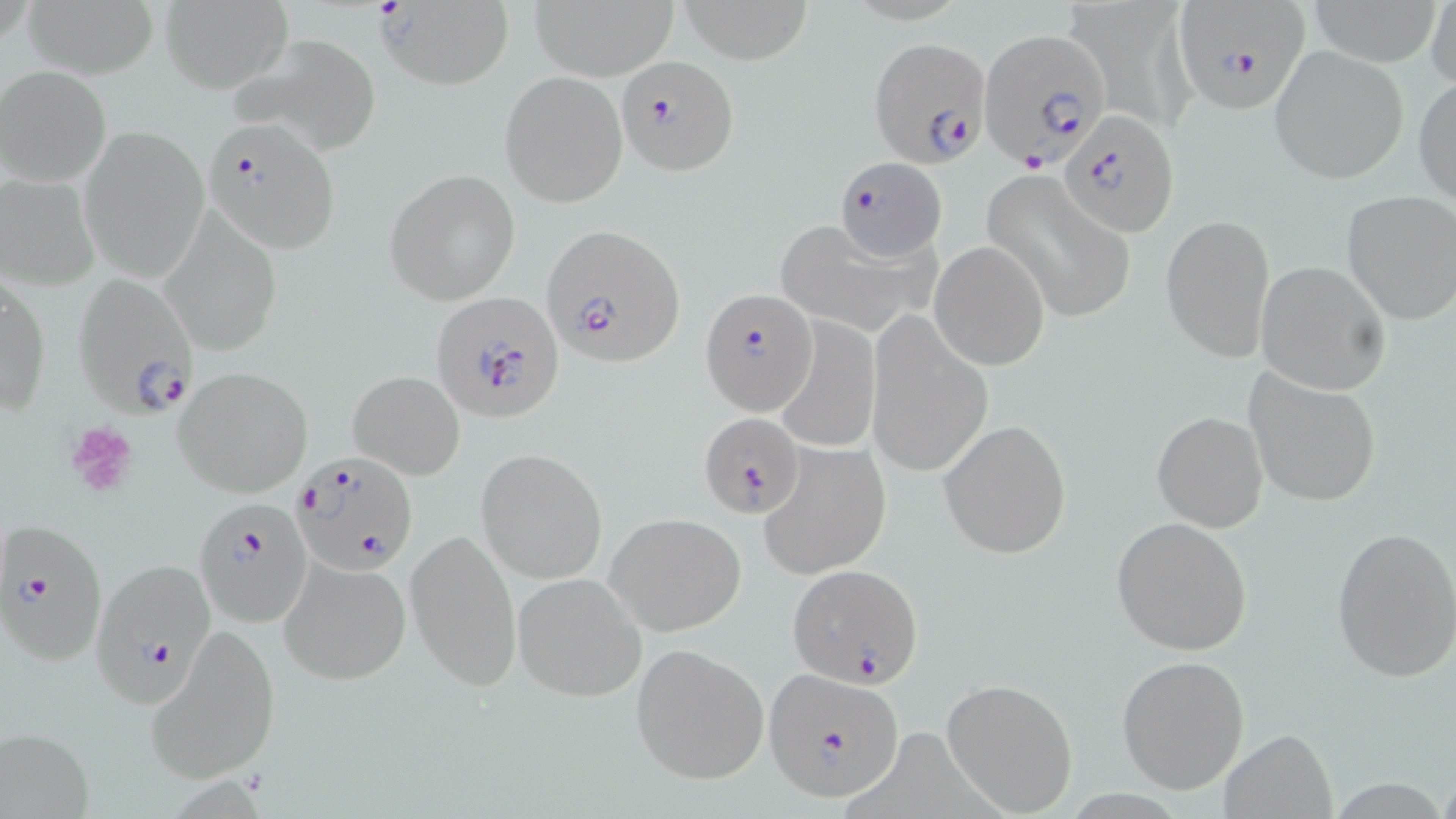

Approximate bounding boxes as [x1, y1, x2, y2] in pixels. Plasmodium falciparum-infected red blood cell locations: [1173, 4, 1312, 113], [977, 27, 1112, 172], [871, 35, 991, 172], [615, 55, 738, 174], [1058, 110, 1179, 236], [202, 119, 340, 253], [832, 158, 947, 260], [539, 223, 684, 367], [70, 272, 200, 418], [702, 288, 818, 415], [430, 294, 567, 423], [698, 414, 803, 519], [293, 450, 418, 575], [194, 496, 313, 626], [0, 519, 109, 666], [88, 555, 218, 704], [787, 563, 925, 688], [762, 668, 906, 802]. Platelet locations: [63, 419, 139, 498]. Uninfected red blood cell locations: [376, 0, 515, 89], [530, 0, 676, 80], [680, 0, 815, 61], [1301, 0, 1447, 66], [1427, 0, 1456, 91], [160, 1, 292, 93], [24, 2, 155, 77], [1074, 2, 1196, 126], [226, 31, 383, 154], [1269, 44, 1408, 186], [1, 65, 112, 187], [500, 72, 627, 206], [1414, 75, 1455, 210], [79, 125, 211, 282], [386, 168, 522, 305], [983, 169, 1139, 323], [0, 173, 99, 289], [1341, 190, 1456, 326], [161, 213, 284, 354], [1160, 214, 1276, 362], [776, 220, 948, 339], [929, 241, 1050, 370], [1254, 259, 1391, 394], [1, 275, 49, 420], [866, 312, 993, 480], [772, 316, 881, 455], [173, 365, 313, 497], [1243, 368, 1384, 509], [348, 370, 466, 480], [1152, 411, 1268, 532], [939, 419, 1073, 559], [760, 440, 891, 581], [474, 449, 608, 584], [606, 512, 746, 636], [1112, 516, 1256, 656], [1330, 525, 1455, 680], [405, 527, 522, 693], [279, 555, 412, 684], [513, 571, 647, 703], [143, 625, 282, 786], [630, 641, 770, 785], [1117, 654, 1252, 795], [940, 678, 1077, 815], [843, 725, 1018, 819], [2, 727, 96, 818], [1219, 730, 1338, 817]. Slide-level diagnosis: Plasmodium falciparum. One field of a larger specimen. May-Grünwald-Giemsa-stained preparation. Image is 1456×819 pixels. Thin blood smear. 1000x magnification. Optical microscopy.